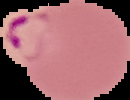

Summary:
  - Result: malaria parasites detected
  - Image type: segmented cell region on a black background
  - Preparation: thin blood smear
  - Image size: 130×100 pixels